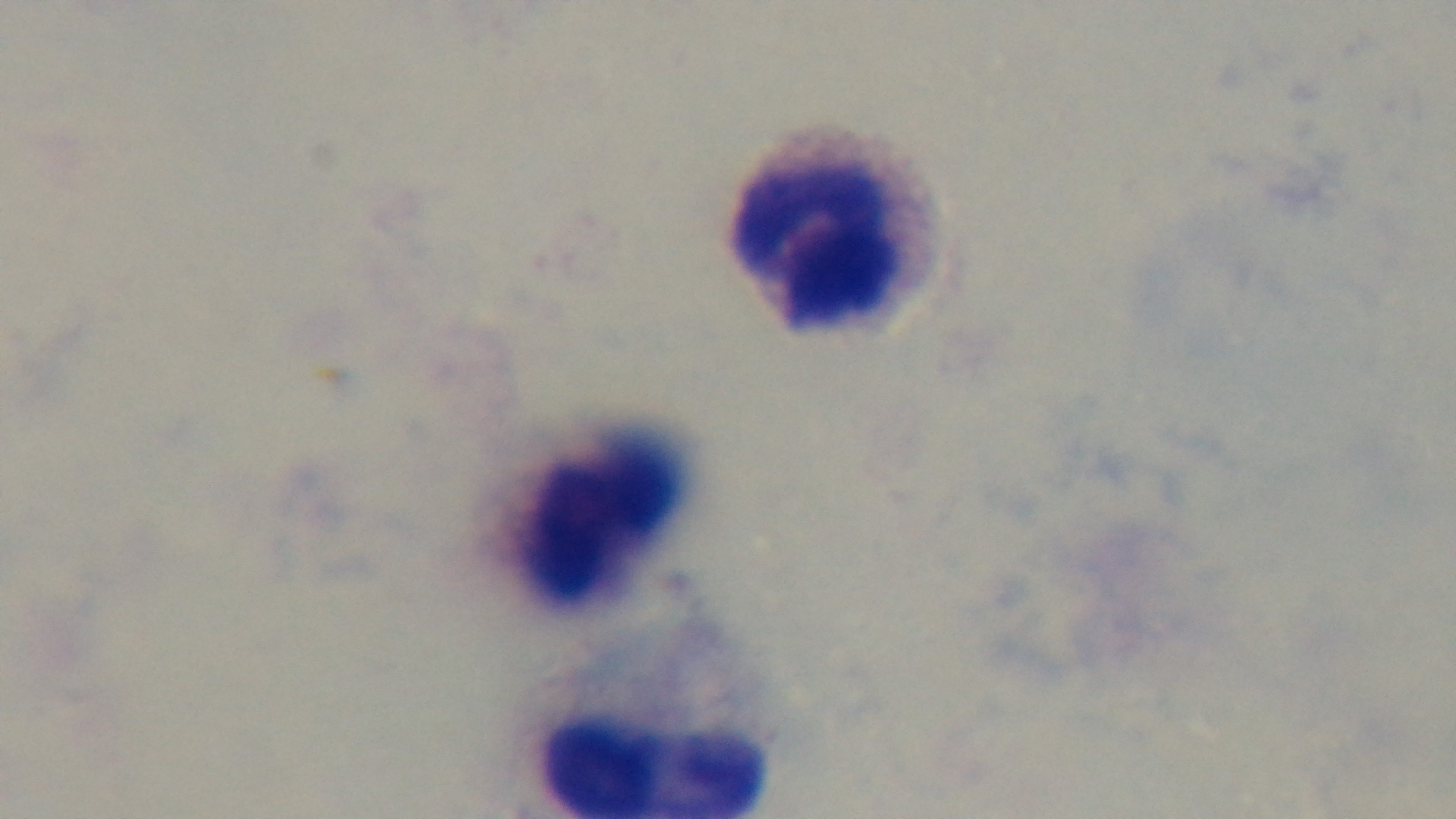

One field from the slide. Photomicrograph. Giemsa-stained. 100x oil-immersion objective. Mounted 4K digital camera. Preparation: thick smear. Malaria status: negative.